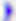
Micrograph. Captured at 400x magnification. Toxoplasma gondii is shown.